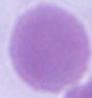
identification = erythrocyte
modality = photomicrograph
magnification = 1000x